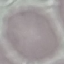 Malaria status: uninfected. Automatically extracted cell patch, resized to 64 × 64 pixels. Acquired by smartphone through the microscope eyepiece. Giemsa-stained preparation. Thin blood smear.